State which parasite is depicted.
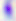
Toxoplasma gondii.

Captured at 400x magnification. Micrograph.